Identify the cell.
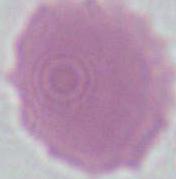

An erythrocyte.

Micrograph. 1000x magnification.